Evaluate for parasitized red blood cells.
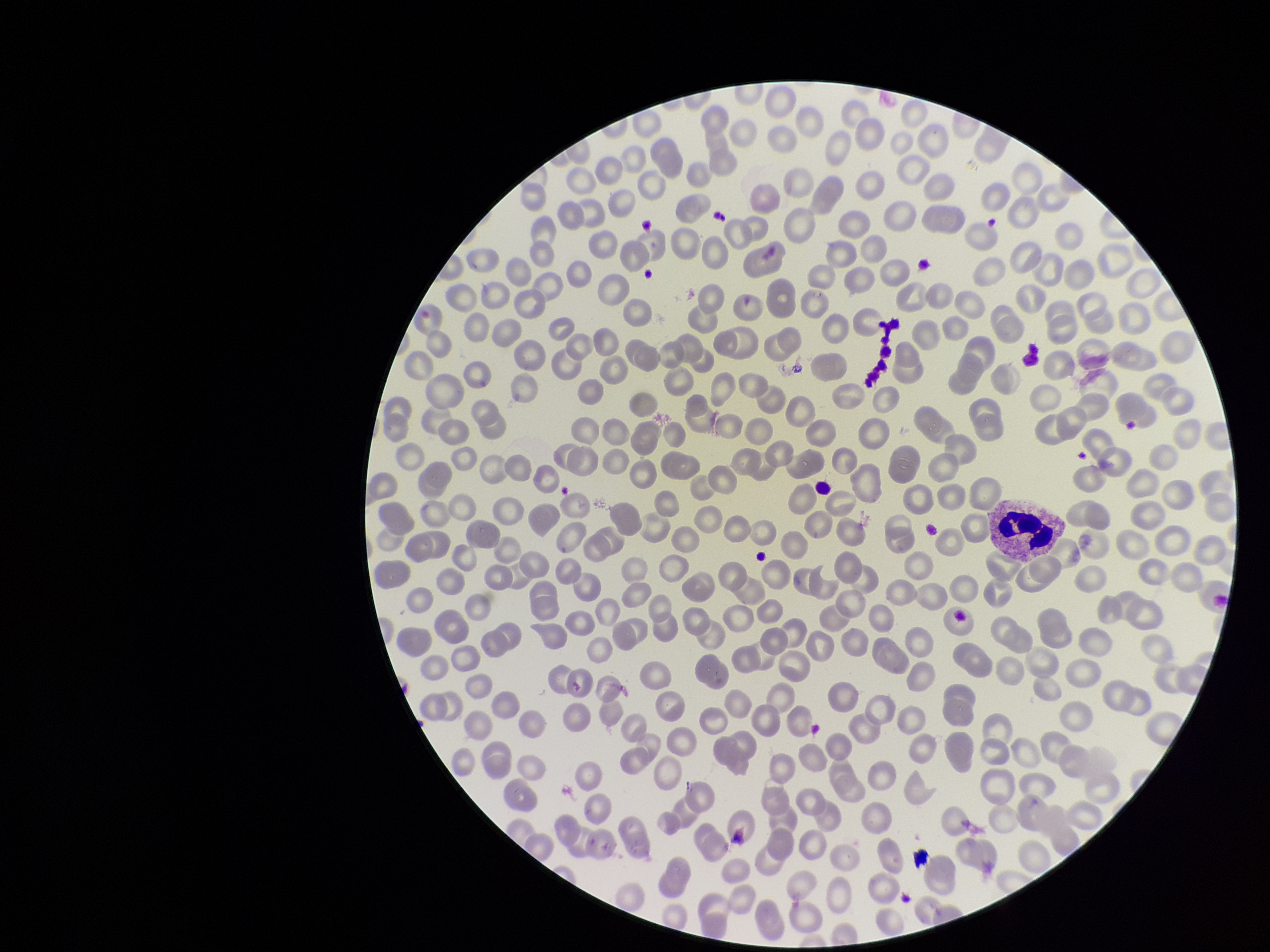
None seen.

parasitized red blood cell count = 0
red blood cell count = 263
preparation = thin blood smear
capture = smartphone photograph through the microscope eyepiece
image size = 1270×952 pixels
stain = Giemsa
field of view = single
patient malaria status = negative